Describe the morphology of the erythrocytes.
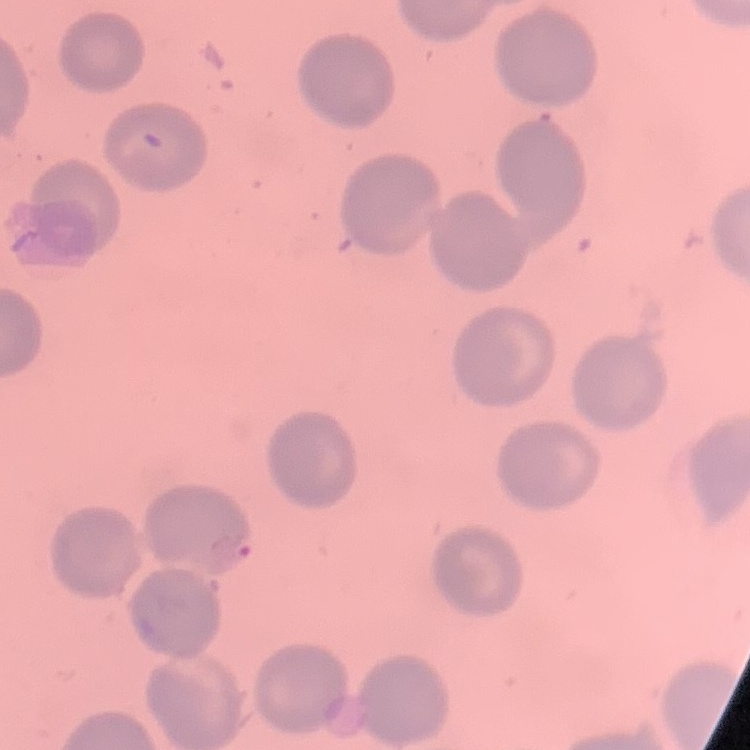

No rouleaux formation.

image type = one tile cut from a larger photomicrograph
preparation = thin blood film
stain = Field's or Giemsa